Give the position of every leukocyte.
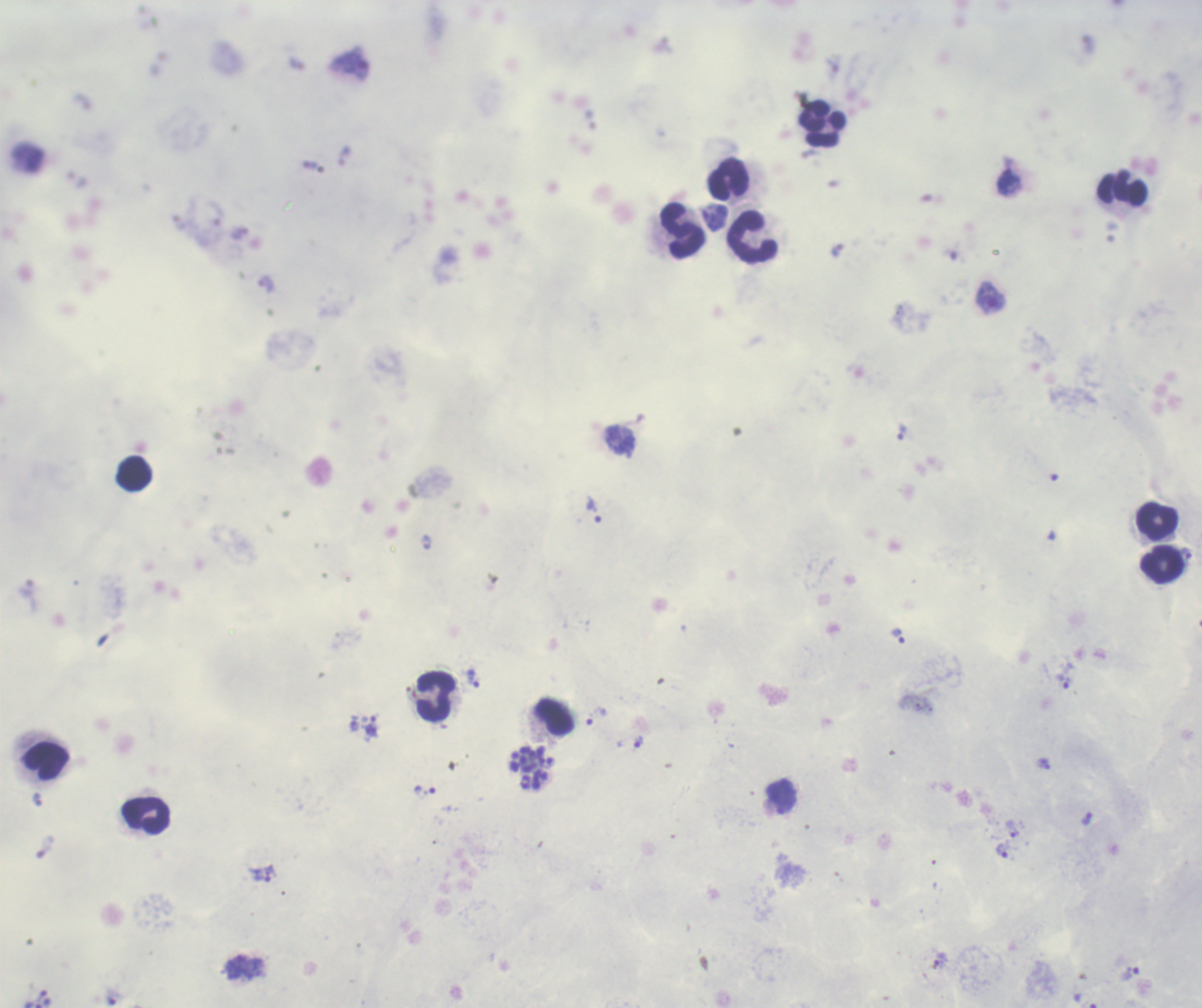

Approximate centers as {x, y} in pixels.
Leukocytes: {823, 124}, {729, 179}, {1122, 189}, {682, 230}, {752, 237}, {135, 472}, {1157, 521}, {1162, 564}, {436, 696}, {554, 716}, {46, 760}, {146, 816}.

Approximate centers as {x, y} in pixels.
Summary:
  - Trophozoite locations: {1009, 181}, {714, 217}, {991, 298}, {902, 432}, {594, 509}, {1186, 553}, {899, 636}, {472, 678}, {1064, 682}, {597, 715}, {372, 725}, {639, 742}, {1044, 764}, {1012, 829}, {1002, 850}, {941, 959}, {1130, 973}
  - Schizont locations: {531, 769}
  - Life-cycle stages observed: trophozoite, schizont
  - Image size: 1202×1008 pixels
  - Magnification: 100x
  - Background quality: good
  - Coloration quality: good
  - Stain: Romanowsky
  - Result: positive for Plasmodium parasites
  - Preparation: thick blood film
  - Field of view: one from this slide
  - Context: previously used in a real diagnosis